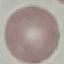
malaria status = uninfected
stain = Giemsa
image type = automatically extracted cell patch, resized to 64 × 64 pixels
capture = smartphone through the microscope eyepiece
preparation = thin smear